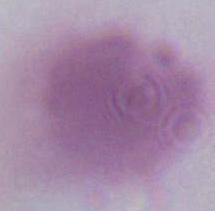
{
  "modality": "photomicrograph",
  "identification": "erythrocyte",
  "magnification": "1000x"
}